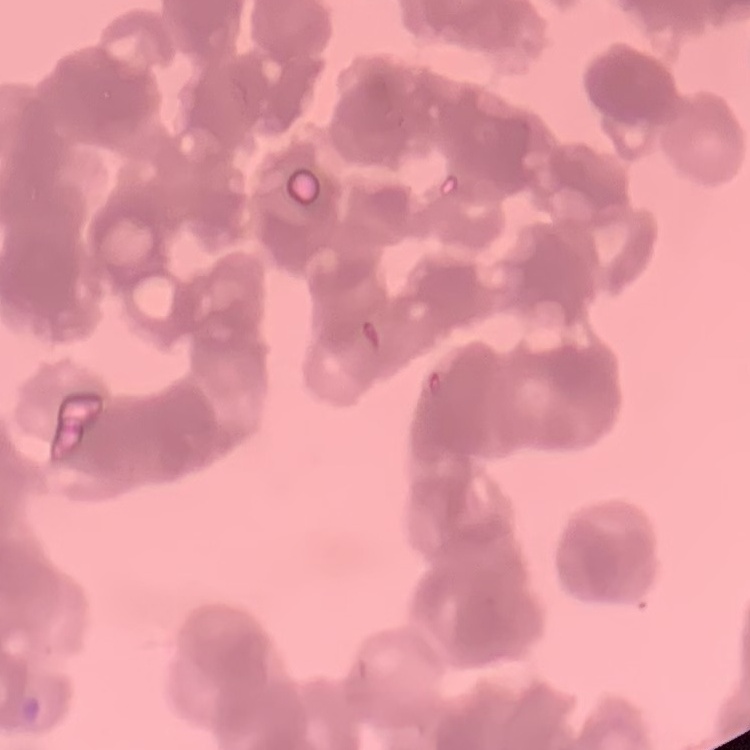

Summary:
  - Erythrocyte morphology: rouleaux formation
  - Preparation: thin blood film
  - Stain: Field's or Giemsa
  - Image type: square crop of a larger photomicrograph